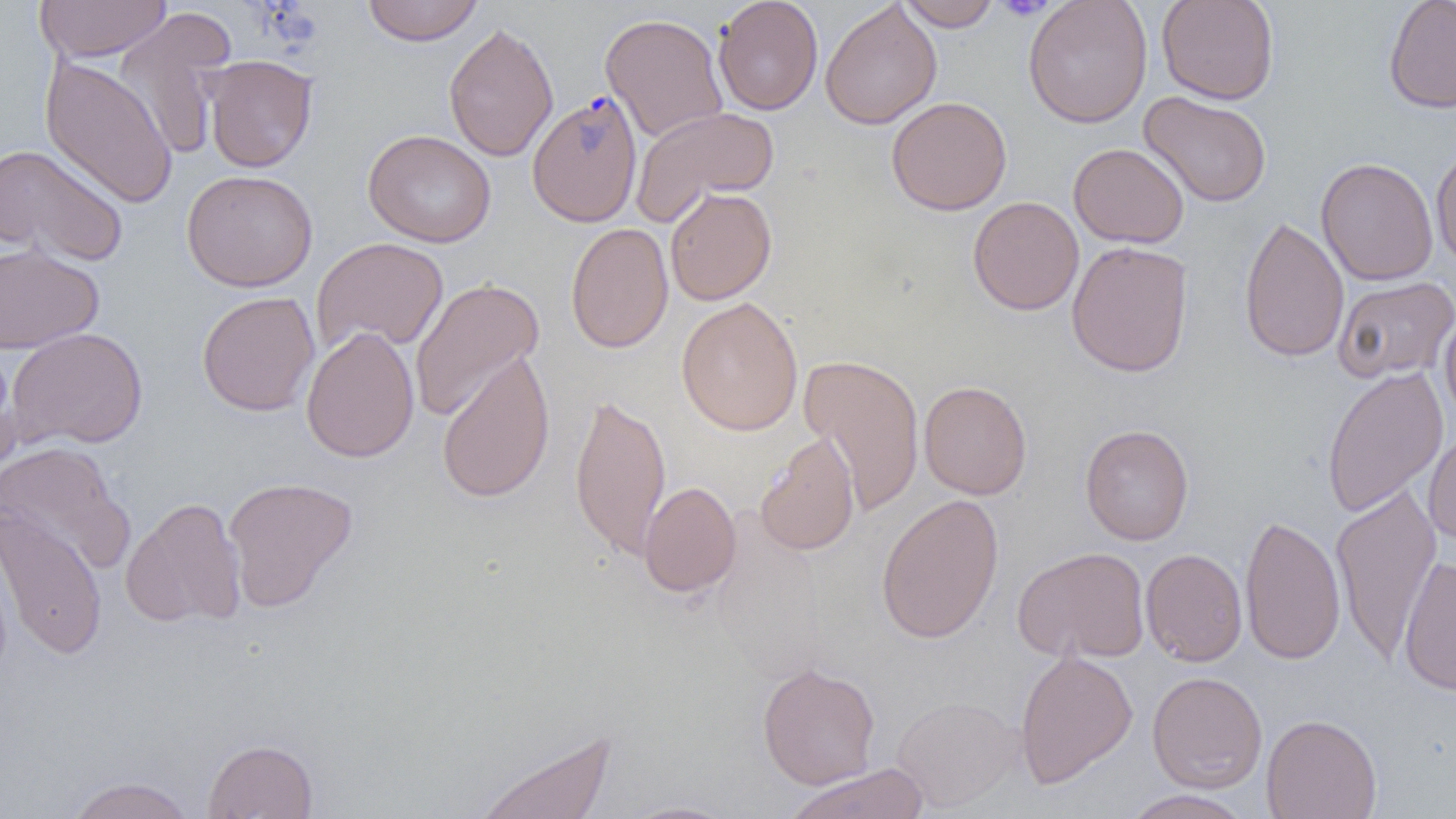

Approximate bounding boxes as named x1/y1/x2/y2 corners in pixels. Uninfected red blood cell locations: (x1=34, y1=0, x2=171, y2=62), (x1=362, y1=0, x2=484, y2=46), (x1=713, y1=0, x2=823, y2=115), (x1=897, y1=0, x2=1002, y2=31), (x1=1023, y1=0, x2=1153, y2=128), (x1=1157, y1=0, x2=1279, y2=105), (x1=1383, y1=0, x2=1456, y2=114), (x1=820, y1=1, x2=942, y2=130), (x1=113, y1=8, x2=238, y2=159), (x1=599, y1=12, x2=729, y2=143), (x1=443, y1=21, x2=559, y2=163), (x1=40, y1=55, x2=178, y2=210), (x1=203, y1=55, x2=318, y2=173), (x1=1138, y1=91, x2=1272, y2=208), (x1=886, y1=96, x2=1012, y2=216), (x1=630, y1=105, x2=780, y2=226), (x1=362, y1=129, x2=496, y2=248), (x1=0, y1=143, x2=128, y2=267), (x1=1068, y1=143, x2=1188, y2=248), (x1=1431, y1=145, x2=1456, y2=271), (x1=1316, y1=157, x2=1439, y2=286), (x1=181, y1=169, x2=318, y2=292), (x1=664, y1=187, x2=777, y2=306), (x1=968, y1=196, x2=1084, y2=316), (x1=1239, y1=215, x2=1349, y2=363), (x1=565, y1=222, x2=674, y2=354), (x1=311, y1=237, x2=449, y2=357), (x1=1066, y1=240, x2=1194, y2=377), (x1=0, y1=242, x2=104, y2=354), (x1=1333, y1=276, x2=1456, y2=383), (x1=409, y1=277, x2=544, y2=422), (x1=197, y1=291, x2=320, y2=417), (x1=676, y1=297, x2=804, y2=436), (x1=1439, y1=309, x2=1456, y2=428), (x1=301, y1=326, x2=420, y2=463), (x1=6, y1=327, x2=149, y2=450), (x1=0, y1=347, x2=21, y2=483), (x1=436, y1=350, x2=556, y2=504), (x1=800, y1=353, x2=925, y2=515), (x1=1321, y1=364, x2=1449, y2=519), (x1=918, y1=380, x2=1032, y2=500), (x1=569, y1=393, x2=671, y2=561), (x1=1079, y1=424, x2=1195, y2=545), (x1=1423, y1=429, x2=1456, y2=546), (x1=754, y1=432, x2=861, y2=556), (x1=0, y1=441, x2=133, y2=573), (x1=222, y1=476, x2=359, y2=612), (x1=639, y1=481, x2=741, y2=598), (x1=1330, y1=484, x2=1442, y2=663), (x1=876, y1=494, x2=1005, y2=644), (x1=121, y1=497, x2=246, y2=629), (x1=0, y1=506, x2=108, y2=661), (x1=1240, y1=512, x2=1346, y2=665), (x1=1012, y1=546, x2=1150, y2=664), (x1=1141, y1=548, x2=1248, y2=667), (x1=1398, y1=556, x2=1456, y2=697), (x1=1014, y1=648, x2=1138, y2=788), (x1=757, y1=661, x2=880, y2=789), (x1=1147, y1=671, x2=1267, y2=793), (x1=890, y1=695, x2=1024, y2=813), (x1=1261, y1=713, x2=1382, y2=819), (x1=474, y1=726, x2=617, y2=819), (x1=202, y1=737, x2=318, y2=818), (x1=784, y1=763, x2=931, y2=819), (x1=64, y1=776, x2=197, y2=819), (x1=1121, y1=789, x2=1254, y2=819), (x1=616, y1=800, x2=740, y2=819). Platelet locations: (x1=994, y1=0, x2=1055, y2=20). Plasmodium falciparum-infected red blood cell locations: (x1=527, y1=91, x2=643, y2=227). Slide-level diagnosis: Plasmodium falciparum. Optical microscopy. One field of a larger specimen. Image is 1456×819 pixels. Thin blood film. Captured at 1000x magnification.